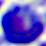 Photomicrograph. A leukocyte is shown. 400x magnification.